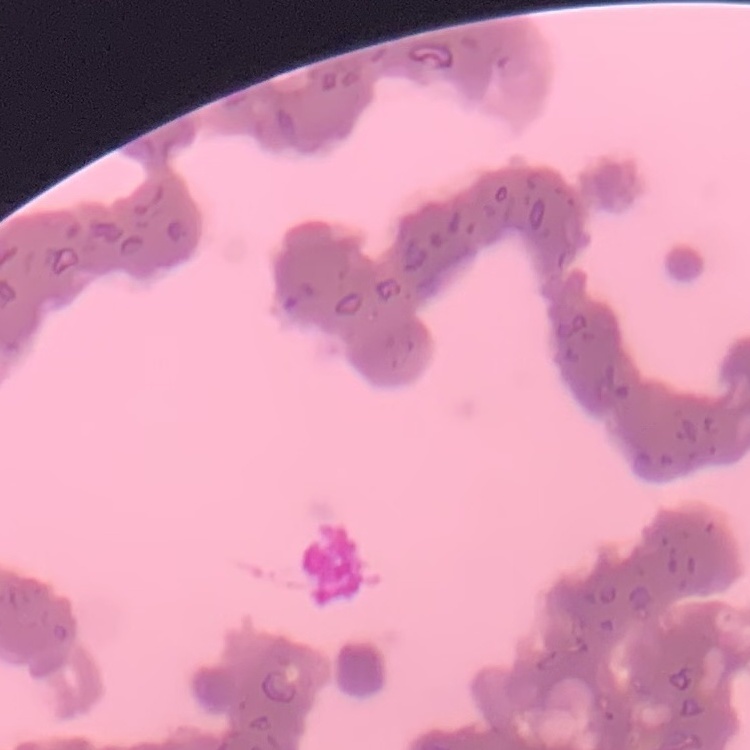
The red blood cells show rouleaux formation. Thin blood smear. One tile cut from a larger photomicrograph. Field's or Giemsa stain.